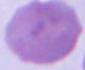
Summary:
  - Magnification: 1000x
  - Modality: micrograph
  - Identification: red blood cell